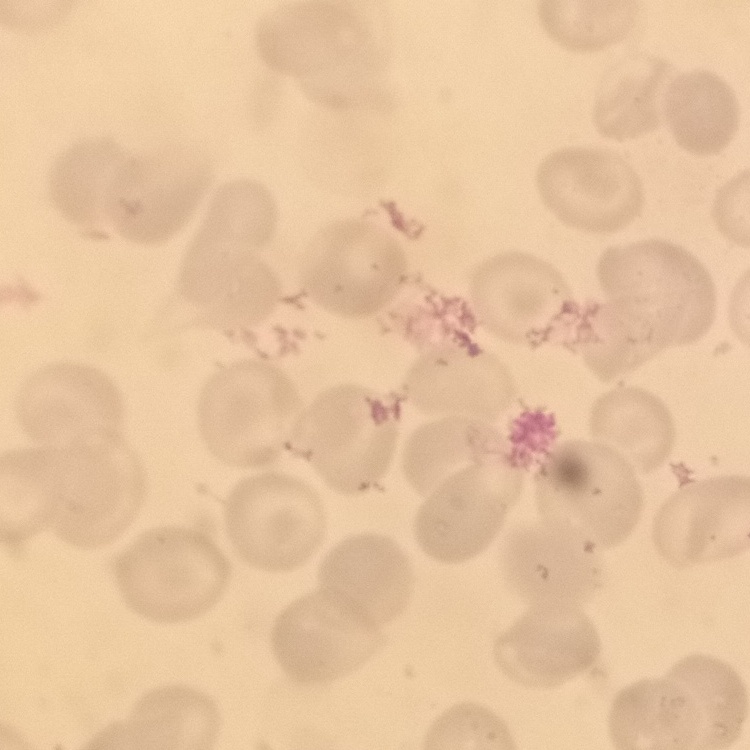 The erythrocytes show no rouleaux formation. Stained with either Field's or Giemsa. Thin peripheral smear. One tile cut from a larger photomicrograph.